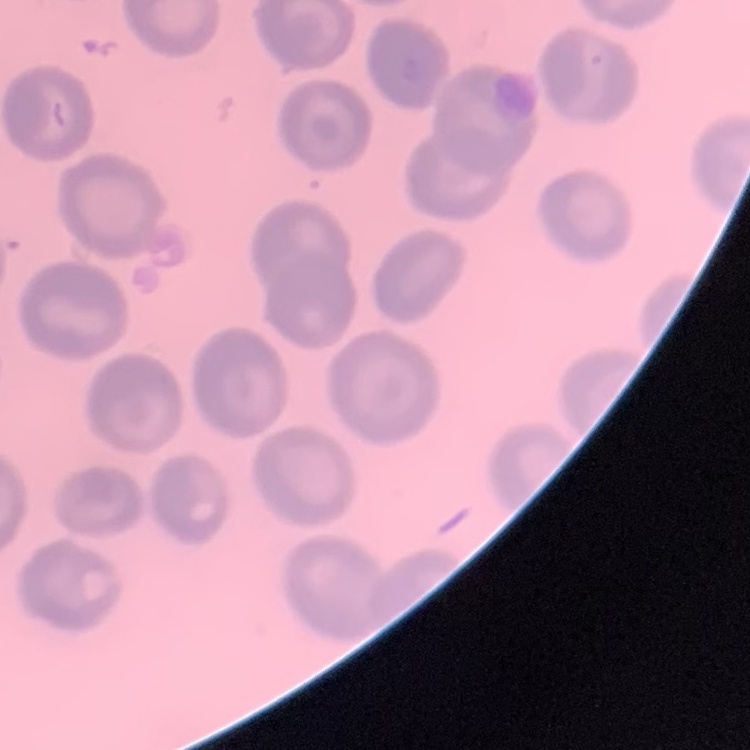
{
  "red_blood_cell_morphology": "no rouleaux formation",
  "stain": "Field's or Giemsa",
  "image_type": "square crop of a larger photomicrograph",
  "preparation": "thin blood smear"
}